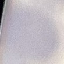 Result: negative for malaria parasites. Automatically extracted cell patch, resized to 64 × 64 pixels. Acquired by smartphone through the microscope eyepiece. Giemsa stain. Thin blood smear.